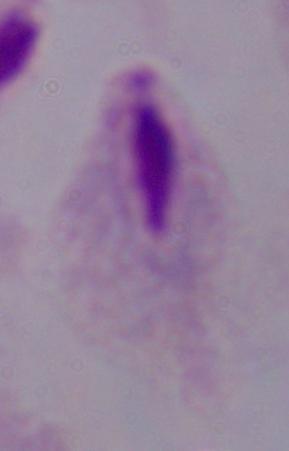

Captured at 1000x magnification. A trichomonad is seen. Micrograph.